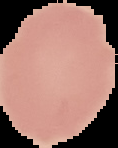
preparation = thin blood smear
image type = segmented cell region on a black background
image size = 118×148 pixels
result = negative for Plasmodium parasites